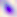

modality = micrograph
identification = Toxoplasma gondii
magnification = 400x